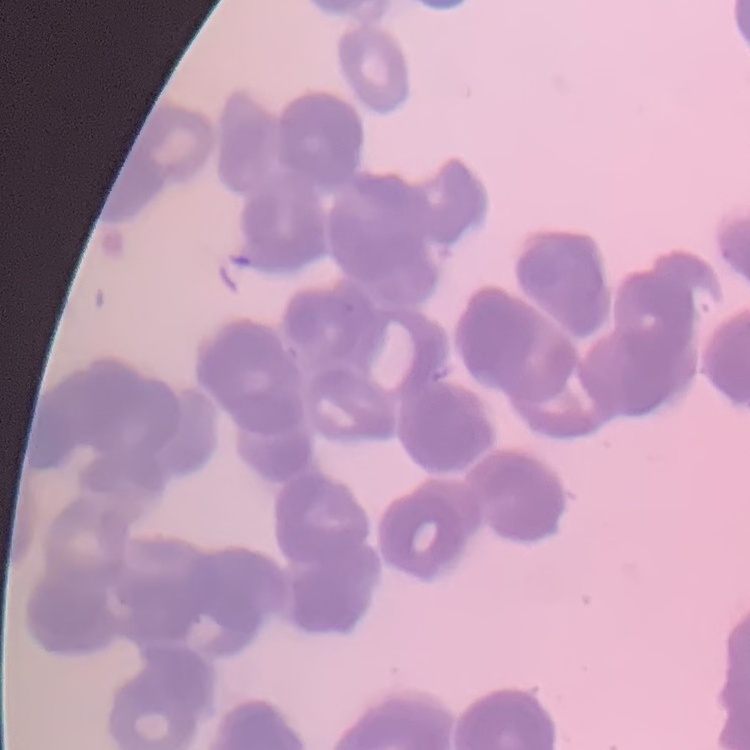
Summary:
  - Red blood cell morphology: rouleaux formation
  - Image type: one tile cut from a larger photomicrograph
  - Preparation: thin blood smear
  - Stain: Field's or Giemsa